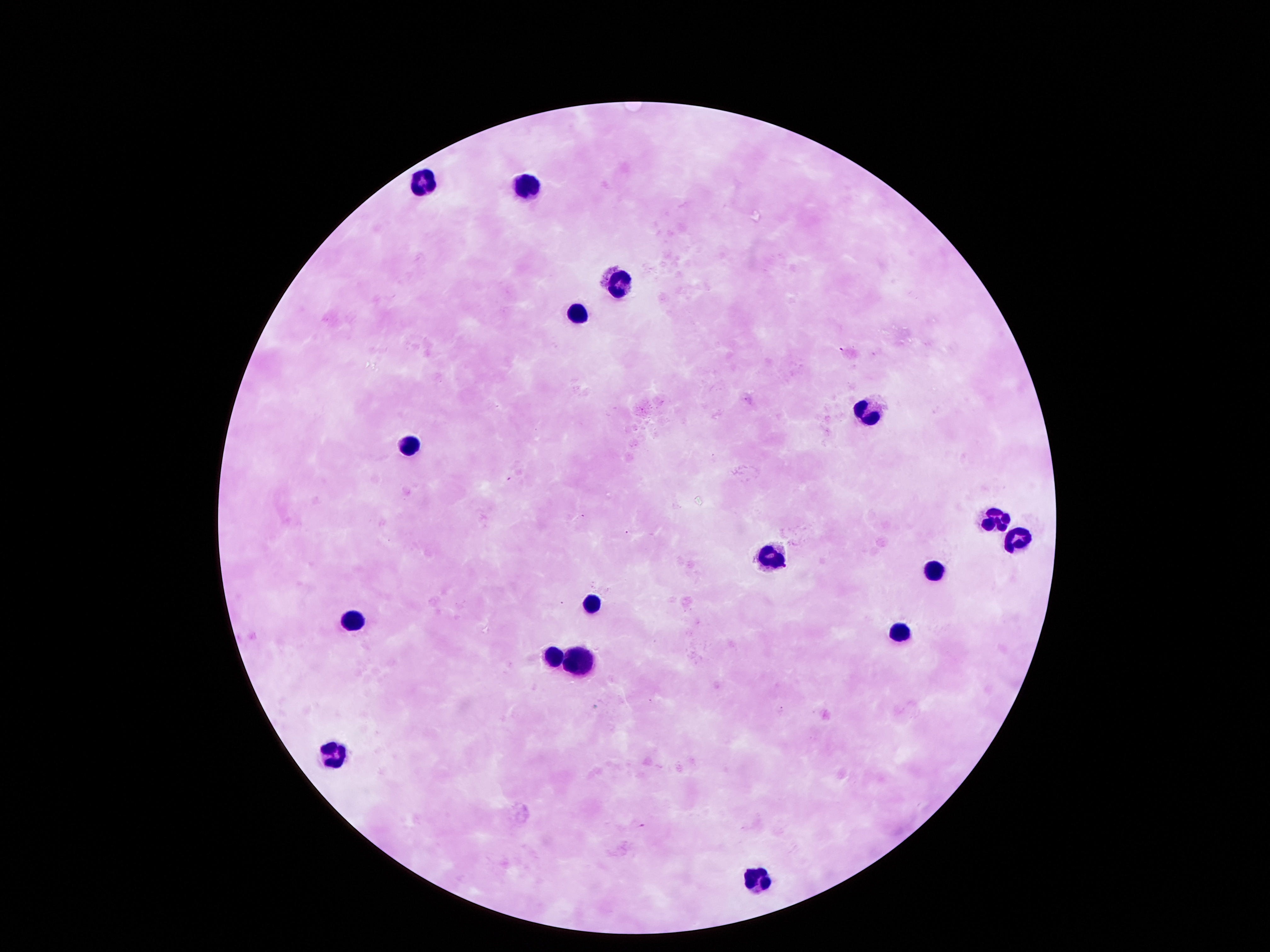

Approximate centers as (x, y) in pixels.
Summary:
  - Leukocyte locations: (424, 181), (528, 185), (615, 276), (575, 316), (867, 410), (407, 442), (992, 514), (1012, 544), (773, 554), (931, 568), (592, 601), (350, 620), (901, 628), (555, 655), (578, 662), (329, 752), (760, 877)
  - Capture: smartphone camera through the microscope eyepiece
  - Stain: Giemsa
  - Magnification: 100x
  - Image size: 1270×952 pixels
  - Field of view: single
  - Patient malaria status: negative
  - Preparation: thick blood film